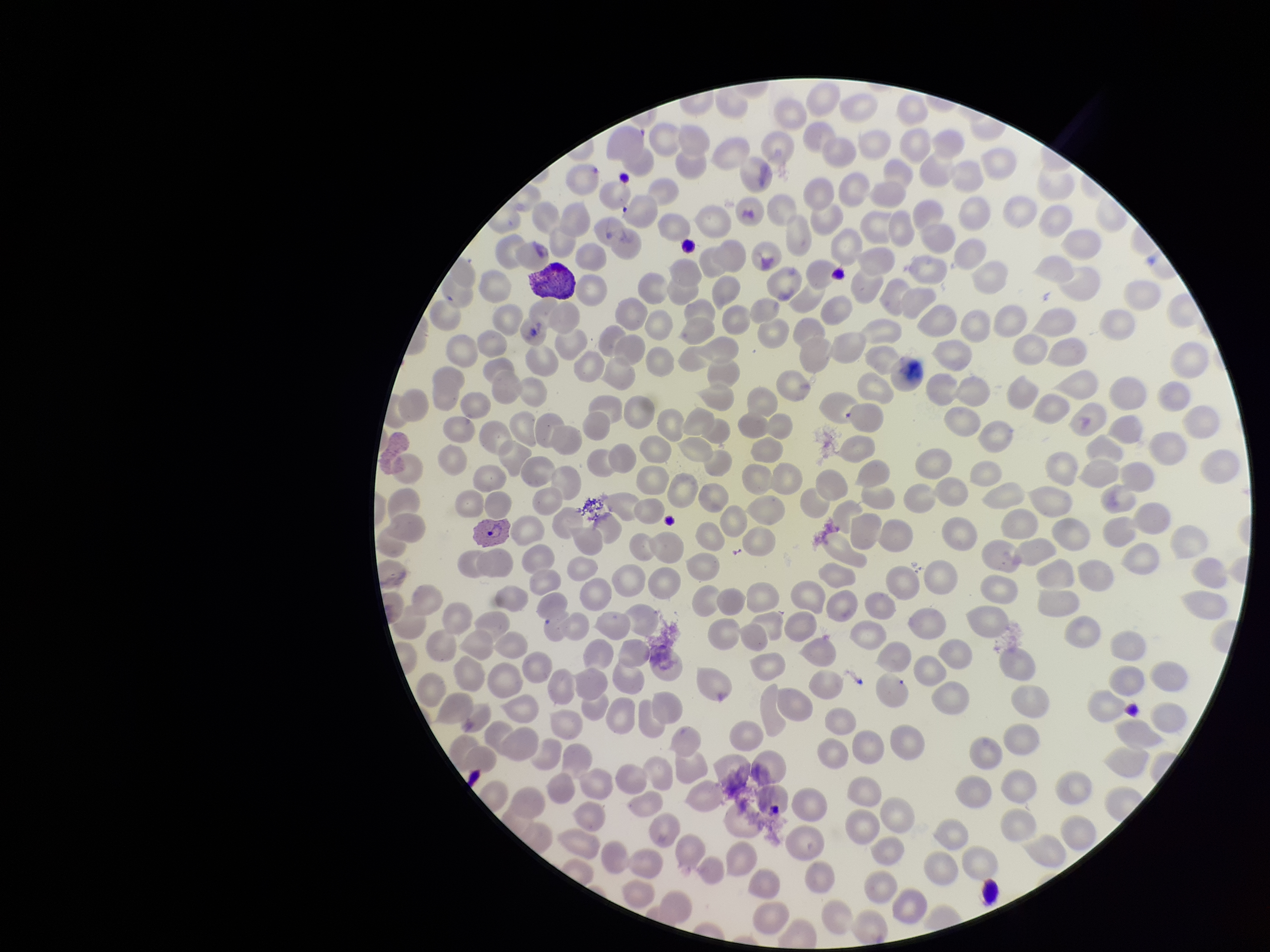
Preparation: thin blood smear. Parasitized red blood cell count: 1. Patient malaria status: infected. Species reported for this patient: Plasmodium vivax. Stained with Giemsa. Image is 1270×952 pixels. Single field of view. Red blood cell count: 254. Smartphone photograph taken through the eyepiece of a microscope. Parasitized red blood cells: detected.